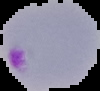
{
  "image_type": "segmented cell region with the area outside set to black",
  "malaria_status": "parasitized",
  "image_size": "100×91 pixels",
  "preparation": "thin blood film"
}